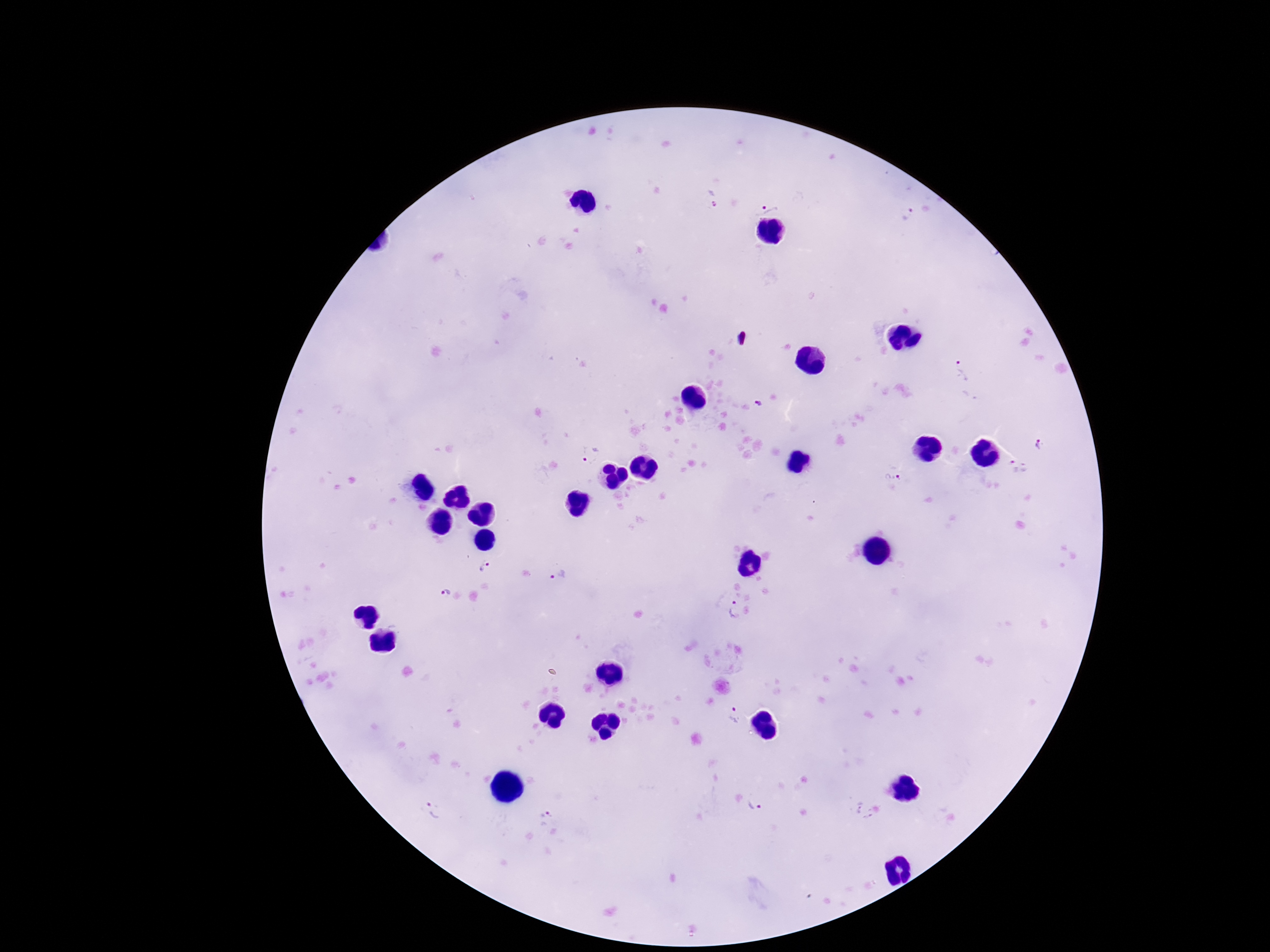

Approximate object centers, in pixels from the top-left corner. Plasmodium parasite locations: (x=763, y=201), (x=908, y=214), (x=964, y=369), (x=1038, y=443), (x=590, y=455), (x=1014, y=466), (x=894, y=476), (x=489, y=568), (x=558, y=577), (x=445, y=591), (x=736, y=610), (x=730, y=714), (x=755, y=804), (x=438, y=809), (x=546, y=814). Single field of view. Patient malaria status: positive. Image is 1270×952 pixels. Giemsa-stained preparation. Thick blood film. Photographed through the microscope eyepiece with a smartphone camera. 100x magnification.